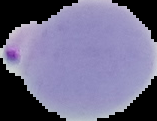

Summary:
  - Preparation: thin blood film
  - Malaria status: parasitized
  - Image size: 157×121 pixels
  - Image type: segmented cell region with the area outside set to black